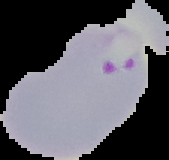

Summary:
  - Image type: cell region segmented out of the field of view; surrounding area masked to black
  - Result: malaria parasites detected
  - Image size: 169×160 pixels
  - Preparation: thin blood film